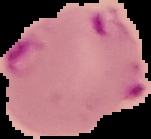

preparation: thin blood film
image_type: segmented cell region with the area outside set to black
result: malaria parasites identified
image_size: 151×139 pixels